Assess this cell for malaria.
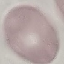
It is uninfected.

Acquired by smartphone through the microscope eyepiece. Cell patch, automatically extracted from a larger field of view and resized to 64 × 64 pixels. Giemsa-stained preparation. Thin blood film.